Report the malaria status of this cell.
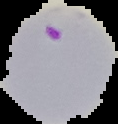

It is parasitized.

Summary:
  - Image size: 118×124 pixels
  - Image type: segmented cell region on a black background
  - Preparation: thin blood smear